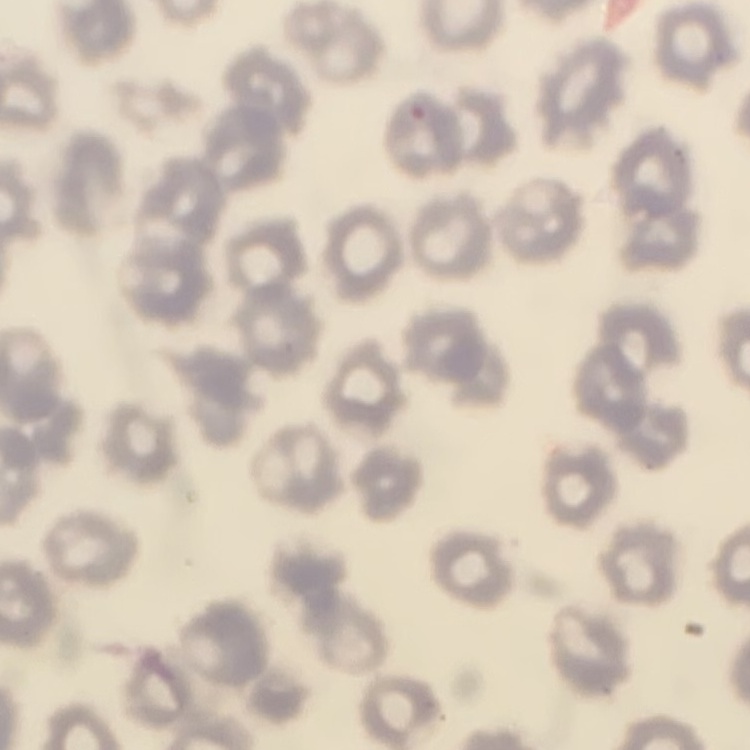

erythrocyte morphology = no rouleaux formation
preparation = thin blood film
stain = Field's or Giemsa
image type = square crop of a larger photomicrograph